Locate and identify every blood parasite.
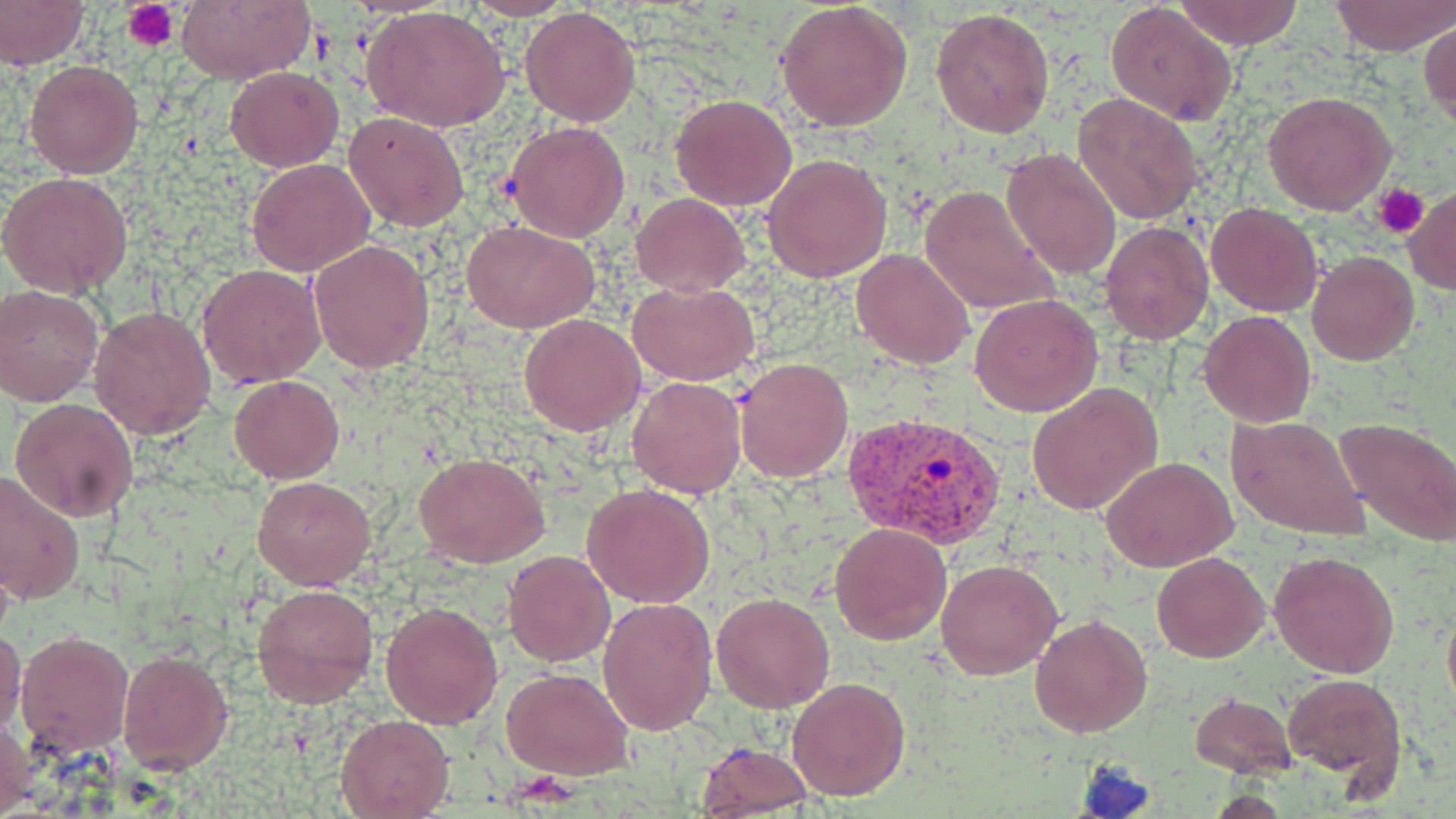
Approximate bounding boxes as (x1,y1)-(x2,y2) corner pairs in pixels.
Plasmodium vivax-infected red blood cells: (845,414)-(1004,548).
No Plasmodium falciparum, Plasmodium ovale, Plasmodium malariae, Babesia divergens, or Trypanosoma brucei observed.

slide-level diagnosis = Plasmodium vivax
modality = optical microscopy
magnification = 1000x
uninfected red blood cell locations = approximate bounding boxes as (x1,y1)-(x2,y2) corner pairs in pixels: (0,0)-(87,68), (174,0)-(316,83), (463,0)-(576,21), (1174,0)-(1305,49), (1332,0)-(1454,55), (775,3)-(913,133), (1105,3)-(1237,127), (520,6)-(640,126), (363,7)-(513,132), (931,8)-(1054,139), (1419,20)-(1454,125), (24,59)-(144,178), (226,66)-(343,171), (1262,91)-(1396,214), (1072,92)-(1204,224), (671,94)-(797,210), (343,110)-(469,231), (505,120)-(631,243), (1001,148)-(1122,282), (762,153)-(894,282), (248,158)-(376,276), (1,172)-(133,297), (920,183)-(1059,317), (1404,189)-(1456,292), (632,193)-(748,295), (1207,202)-(1322,317), (463,220)-(599,332), (1099,220)-(1214,345), (308,239)-(435,372), (851,249)-(975,368), (1306,251)-(1420,365), (198,265)-(325,386), (630,281)-(760,386), (1,286)-(102,406), (970,293)-(1103,417), (89,305)-(218,439), (1198,311)-(1316,428), (519,313)-(645,435), (735,357)-(853,482), (229,375)-(343,482), (627,376)-(746,500), (1028,383)-(1162,516), (10,398)-(139,521), (1226,415)-(1370,542), (1333,417)-(1456,546), (414,454)-(548,568), (1103,457)-(1238,573), (0,473)-(85,607), (252,476)-(376,589), (581,483)-(715,609), (829,521)-(952,646), (503,550)-(614,666), (1268,550)-(1400,678), (1151,551)-(1269,662), (935,560)-(1062,681), (252,582)-(379,707), (711,592)-(835,712), (599,598)-(717,736), (382,602)-(502,728), (1442,607)-(1456,716), (1028,614)-(1152,739), (0,628)-(25,736), (14,630)-(133,756), (116,647)-(234,774), (503,667)-(633,779), (1280,673)-(1406,788), (786,676)-(910,802), (1189,692)-(1298,777), (1,712)-(35,819), (336,714)-(453,818), (697,742)-(814,815)
preparation = thin blood smear
platelet locations = approximate bounding boxes as (x1,y1)-(x2,y2) corner pairs in pixels: (122,0)-(178,49), (1374,183)-(1428,238)
field of view = single
stain = May-Grünwald-Giemsa
image size = 1456×819 pixels